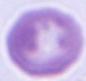

identification: erythrocyte
modality: photomicrograph
magnification: 1000x